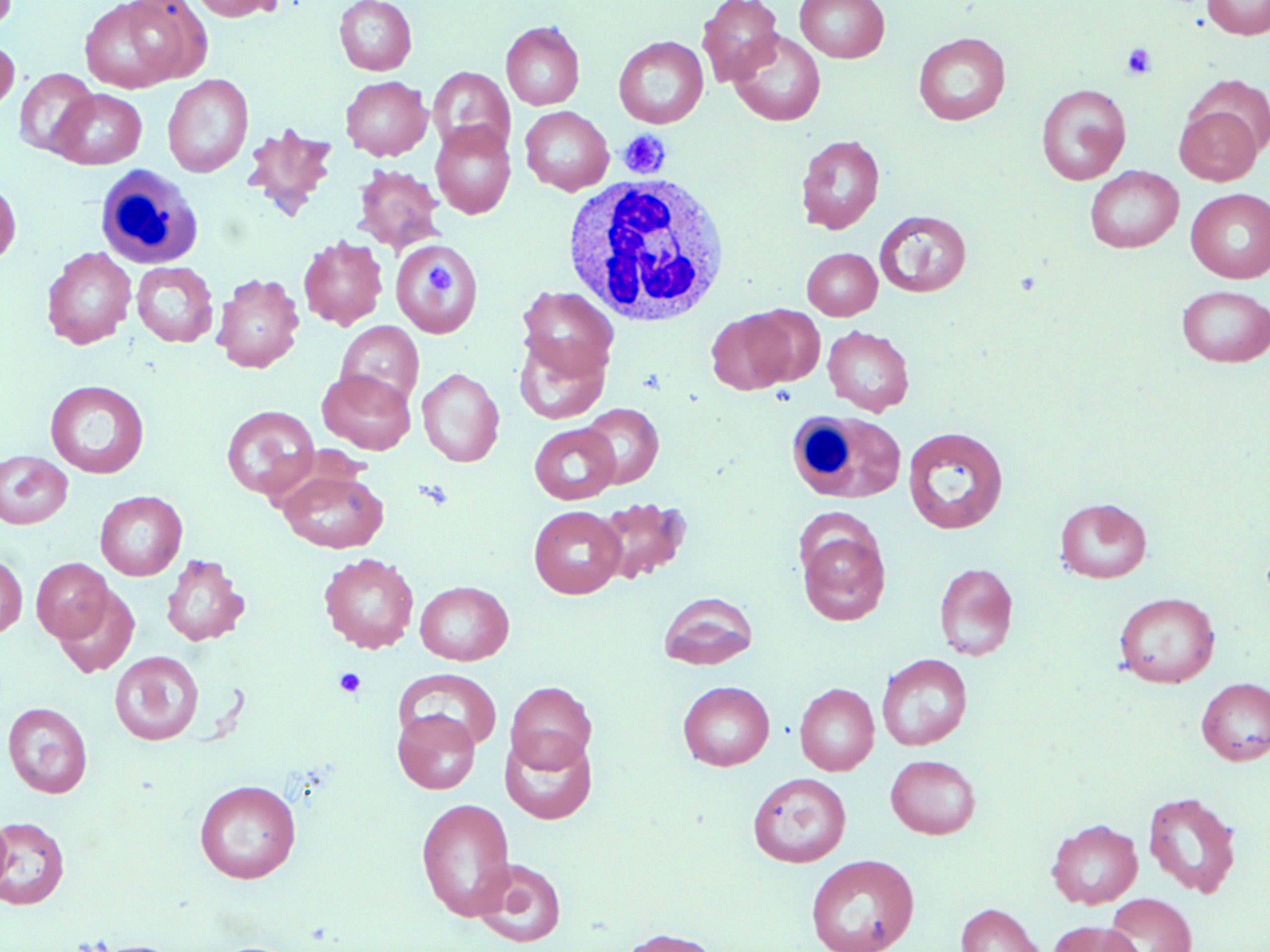

Summary:
  - Coordinate format: approximate bounding boxes as named x1/y1/x2/y2 corners in pixels
  - Platelet locations: (x1=1121, y1=43, x2=1157, y2=79), (x1=618, y1=130, x2=671, y2=179), (x1=424, y1=262, x2=456, y2=298), (x1=414, y1=479, x2=455, y2=509), (x1=334, y1=667, x2=366, y2=697)
  - Uninfected red blood cell locations: (x1=78, y1=0, x2=212, y2=92), (x1=189, y1=0, x2=284, y2=21), (x1=334, y1=0, x2=417, y2=75), (x1=697, y1=0, x2=783, y2=86), (x1=794, y1=0, x2=890, y2=63), (x1=1202, y1=0, x2=1270, y2=40), (x1=501, y1=21, x2=585, y2=110), (x1=729, y1=31, x2=826, y2=126), (x1=913, y1=32, x2=1011, y2=125), (x1=613, y1=36, x2=708, y2=128), (x1=0, y1=37, x2=19, y2=117), (x1=428, y1=66, x2=516, y2=156), (x1=14, y1=68, x2=98, y2=157), (x1=163, y1=74, x2=254, y2=177), (x1=341, y1=76, x2=432, y2=160), (x1=1184, y1=76, x2=1270, y2=160), (x1=1036, y1=84, x2=1131, y2=185), (x1=50, y1=89, x2=146, y2=169), (x1=1174, y1=103, x2=1263, y2=186), (x1=520, y1=106, x2=614, y2=195), (x1=430, y1=121, x2=516, y2=219), (x1=241, y1=123, x2=338, y2=220), (x1=795, y1=134, x2=885, y2=234), (x1=351, y1=164, x2=446, y2=253), (x1=1085, y1=166, x2=1183, y2=253), (x1=0, y1=177, x2=21, y2=268), (x1=1186, y1=189, x2=1270, y2=283), (x1=875, y1=210, x2=971, y2=297), (x1=298, y1=236, x2=387, y2=330), (x1=391, y1=242, x2=483, y2=336), (x1=41, y1=247, x2=137, y2=349), (x1=803, y1=248, x2=882, y2=320), (x1=132, y1=262, x2=218, y2=347), (x1=212, y1=273, x2=304, y2=372), (x1=517, y1=285, x2=619, y2=381), (x1=1176, y1=285, x2=1270, y2=367), (x1=744, y1=305, x2=825, y2=386), (x1=706, y1=310, x2=795, y2=395), (x1=335, y1=321, x2=424, y2=407), (x1=823, y1=325, x2=914, y2=416), (x1=513, y1=335, x2=610, y2=424), (x1=417, y1=368, x2=504, y2=467), (x1=318, y1=369, x2=417, y2=454), (x1=45, y1=380, x2=149, y2=477), (x1=579, y1=403, x2=664, y2=488), (x1=221, y1=405, x2=320, y2=501), (x1=529, y1=423, x2=621, y2=504), (x1=903, y1=425, x2=1009, y2=534), (x1=0, y1=451, x2=72, y2=529), (x1=278, y1=468, x2=389, y2=553), (x1=95, y1=490, x2=187, y2=580), (x1=593, y1=496, x2=691, y2=585), (x1=1054, y1=498, x2=1152, y2=583), (x1=529, y1=505, x2=626, y2=598), (x1=795, y1=517, x2=891, y2=625), (x1=161, y1=552, x2=250, y2=646), (x1=319, y1=552, x2=419, y2=653), (x1=0, y1=554, x2=27, y2=637), (x1=31, y1=557, x2=113, y2=642), (x1=933, y1=562, x2=1018, y2=660), (x1=414, y1=580, x2=514, y2=666), (x1=54, y1=586, x2=139, y2=678), (x1=658, y1=591, x2=759, y2=670), (x1=1114, y1=591, x2=1220, y2=688), (x1=109, y1=650, x2=203, y2=745), (x1=877, y1=654, x2=972, y2=750), (x1=393, y1=668, x2=502, y2=752), (x1=1196, y1=677, x2=1270, y2=766), (x1=506, y1=681, x2=596, y2=772), (x1=678, y1=681, x2=775, y2=770), (x1=794, y1=683, x2=879, y2=775), (x1=3, y1=701, x2=93, y2=798), (x1=392, y1=708, x2=480, y2=794), (x1=499, y1=730, x2=597, y2=824), (x1=885, y1=754, x2=981, y2=839), (x1=747, y1=771, x2=851, y2=868), (x1=194, y1=779, x2=301, y2=882), (x1=1142, y1=791, x2=1242, y2=898), (x1=416, y1=797, x2=516, y2=921), (x1=0, y1=815, x2=11, y2=897), (x1=0, y1=815, x2=70, y2=909), (x1=1046, y1=818, x2=1143, y2=908), (x1=805, y1=854, x2=919, y2=952), (x1=472, y1=858, x2=568, y2=947), (x1=1103, y1=893, x2=1197, y2=952), (x1=955, y1=902, x2=1046, y2=952), (x1=1047, y1=919, x2=1144, y2=952), (x1=615, y1=927, x2=722, y2=952), (x1=86, y1=940, x2=188, y2=952)
  - White blood cell locations: (x1=99, y1=165, x2=208, y2=270), (x1=560, y1=172, x2=732, y2=325), (x1=787, y1=409, x2=906, y2=504)
  - Slide-level diagnosis: no evidence of blood parasites
  - Magnification: 1000x
  - Image size: 1270×952 pixels
  - Preparation: thin blood film
  - Field of view: one of a larger specimen
  - Stain: May-Grünwald-Giemsa
  - Modality: optical microscopy